Name the parasite shown.
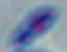
Toxoplasma gondii.

magnification = 1000x
modality = photomicrograph